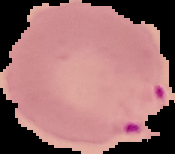

The area outside the segmented cell region is set to black. Image is 175×154 pixels. From a thin blood smear. Malaria status: parasitized.